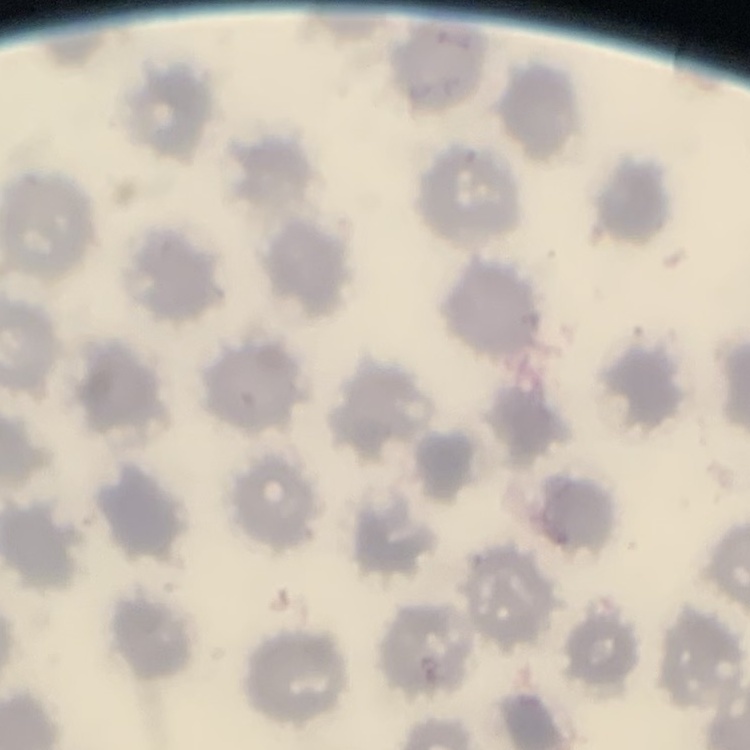
red blood cell morphology = no rouleaux formation
image type = square crop of a larger photomicrograph
stain = Field's or Giemsa
preparation = thin blood film